Assess this cell for malaria.
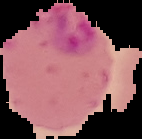

It is parasitized.

Summary:
  - Image type: cell region segmented out of the field of view; surrounding area masked to black
  - Preparation: thin blood smear
  - Image size: 142×139 pixels